Report the malaria status of this cell.
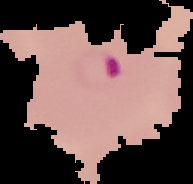

It is parasitized.

From a thin blood film. Cell region segmented out of the field of view; the surrounding area is masked to black. Image is 193×184 pixels.